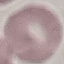 Malaria status: uninfected. Thin blood smear. Cell patch, automatically extracted from a larger field of view and resized to 64 × 64 pixels. Giemsa stain. Photographed with a smartphone camera at the microscope eyepiece.